Report the malaria status of this cell.
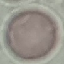
It is uninfected.

preparation = thin smear
image type = cell patch, automatically extracted from a larger field of view and resized to 64 × 64 pixels
stain = Giemsa
capture = smartphone camera at the microscope eyepiece